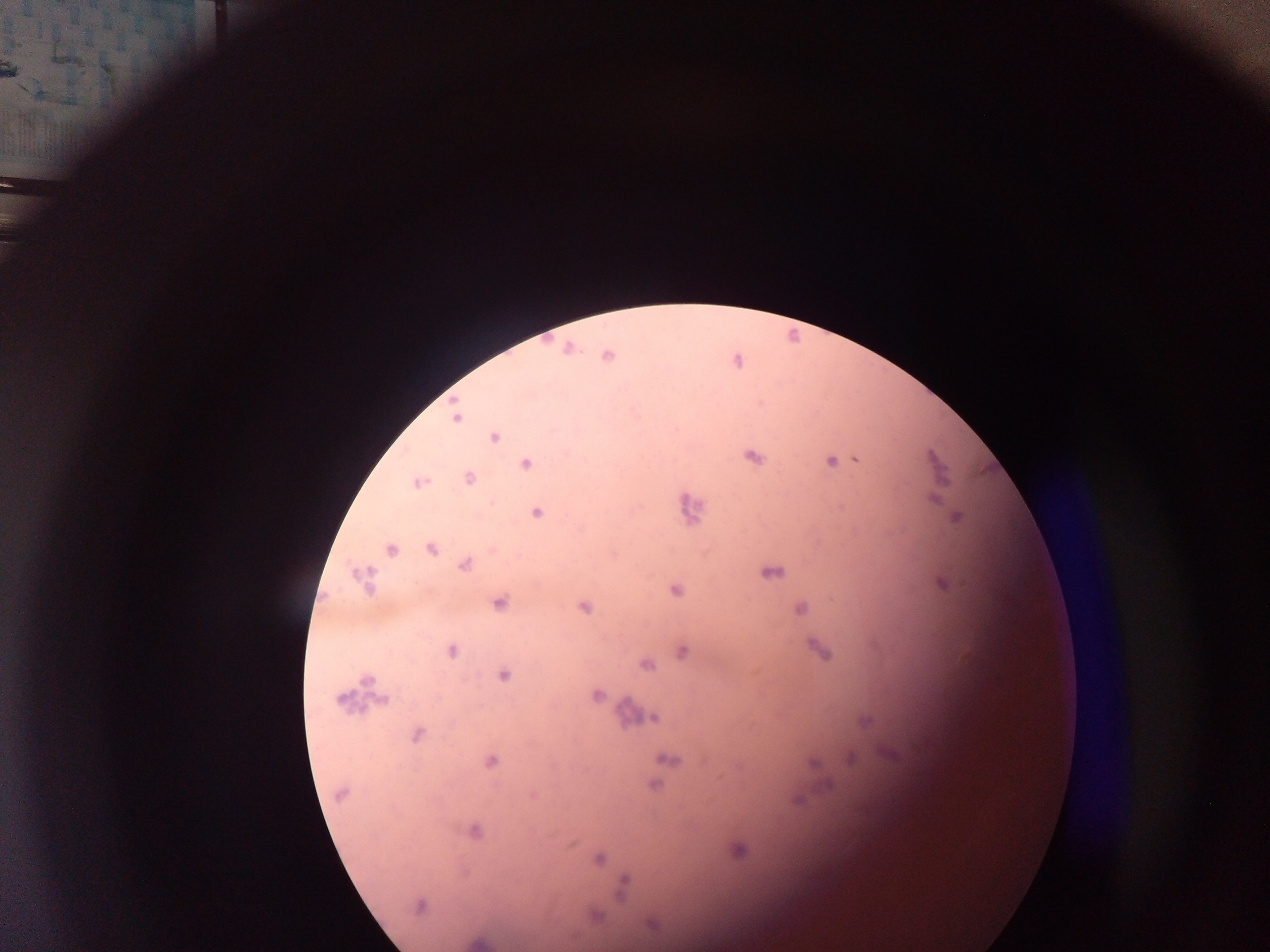

{
  "capture": "mobile-phone photograph through a microscope",
  "malaria_parasite_locations": "approximate centers as [x, y] in pixels: [568, 349], [607, 355], [456, 416], [494, 437], [754, 457], [857, 460], [830, 461], [526, 464], [469, 479], [418, 483], [933, 500], [536, 512], [957, 517], [391, 549], [431, 549], [465, 564], [773, 572], [363, 580], [944, 584], [676, 590], [499, 604], [584, 608], [800, 609], [821, 650], [451, 652], [683, 652], [647, 665], [503, 675], [597, 695], [340, 699], [381, 701], [653, 717], [865, 721], [417, 734], [851, 758], [669, 760], [491, 761], [829, 784], [655, 785], [341, 794], [798, 800], [474, 831], [739, 851], [599, 858], [623, 885], [419, 906], [597, 916]",
  "field_of_view": "single",
  "country": "Ghana",
  "image_size": "1270×952 pixels",
  "preparation": "thick blood film"
}